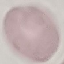

Summary:
  - Malaria status: uninfected
  - Capture: smartphone camera at the microscope eyepiece
  - Stain: Giemsa
  - Preparation: thin smear
  - Image type: cell patch, automatically extracted from a larger field of view and resized to 64 × 64 pixels